Name the parasite shown.
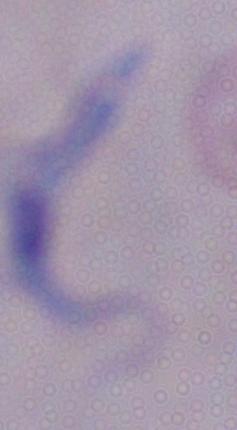

This is a trypanosome.

magnification = 1000x
modality = micrograph